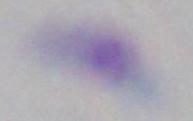
Summary:
  - Magnification: 1000x
  - Modality: micrograph
  - Identification: Toxoplasma gondii